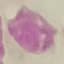
{
  "malaria_status": "uninfected",
  "image_type": "automatically extracted cell patch, resized to 64 × 64 pixels",
  "preparation": "thin smear",
  "stain": "Giemsa",
  "capture": "smartphone camera at the microscope eyepiece"
}